State which parasite is depicted.
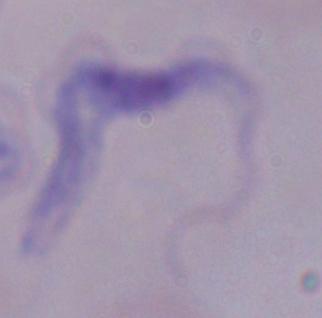

A trypanosome.

modality = micrograph
magnification = 1000x